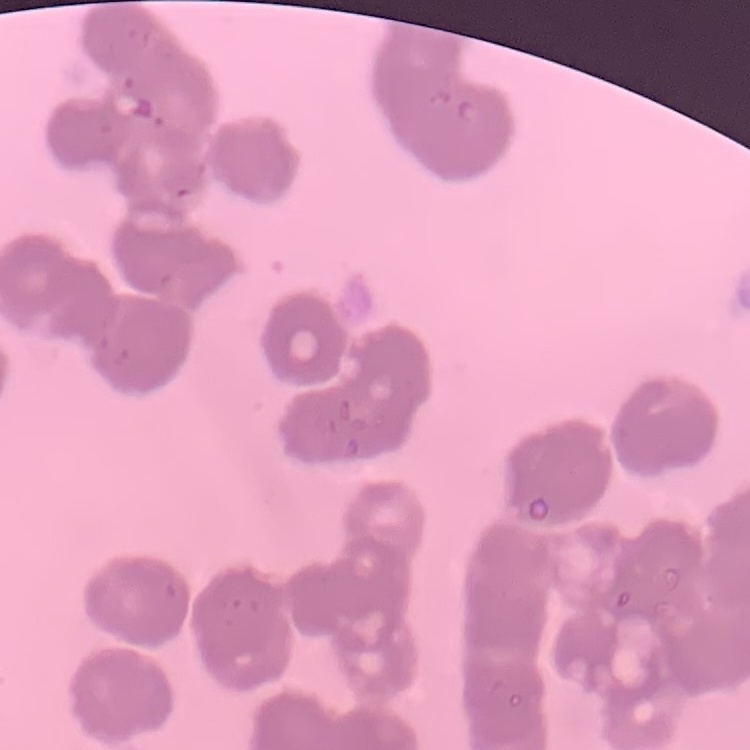

Summary:
  - Erythrocyte morphology: rouleaux formation
  - Stain: Field's or Giemsa
  - Image type: square crop of a larger photomicrograph
  - Preparation: thin blood film